Assess this cell for malaria.
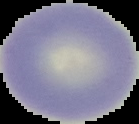

Uninfected.

image_type: segmented cell region on a black background
image_size: 139×124 pixels
preparation: thin blood smear